Locate every malaria parasite.
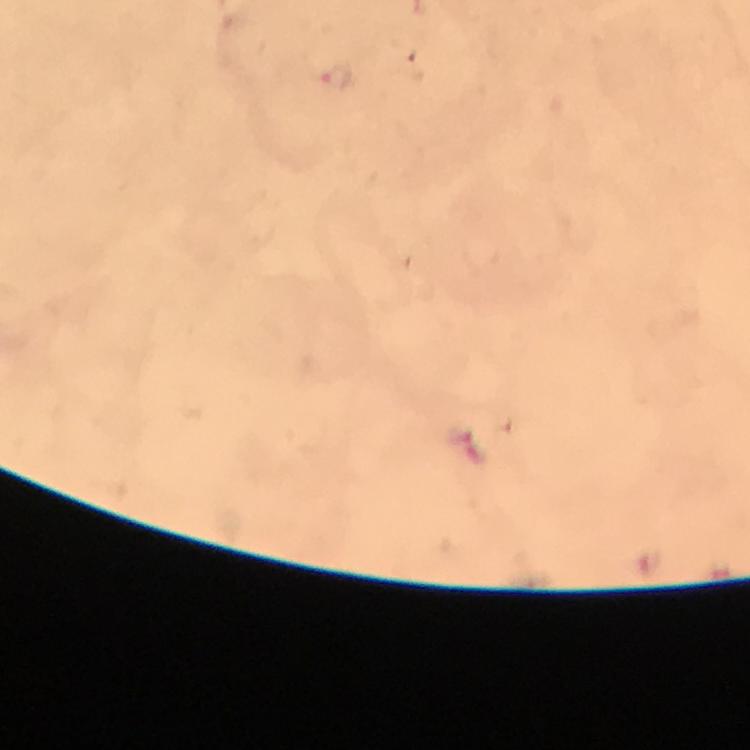

Approximate object centers, in pixels from the top-left corner.
Malaria parasites: (x=335, y=78).

Summary:
  - Capture: smartphone camera through the microscope
  - Cropped from: a single field of view
  - Stain: Giemsa
  - Immersion oil: applied
  - Magnification: 100x
  - Image size: 750×750 pixels
  - Preparation: thick blood smear
  - Context: from a diagnostic examination for malaria